Locate every blood parasite and identify its species.
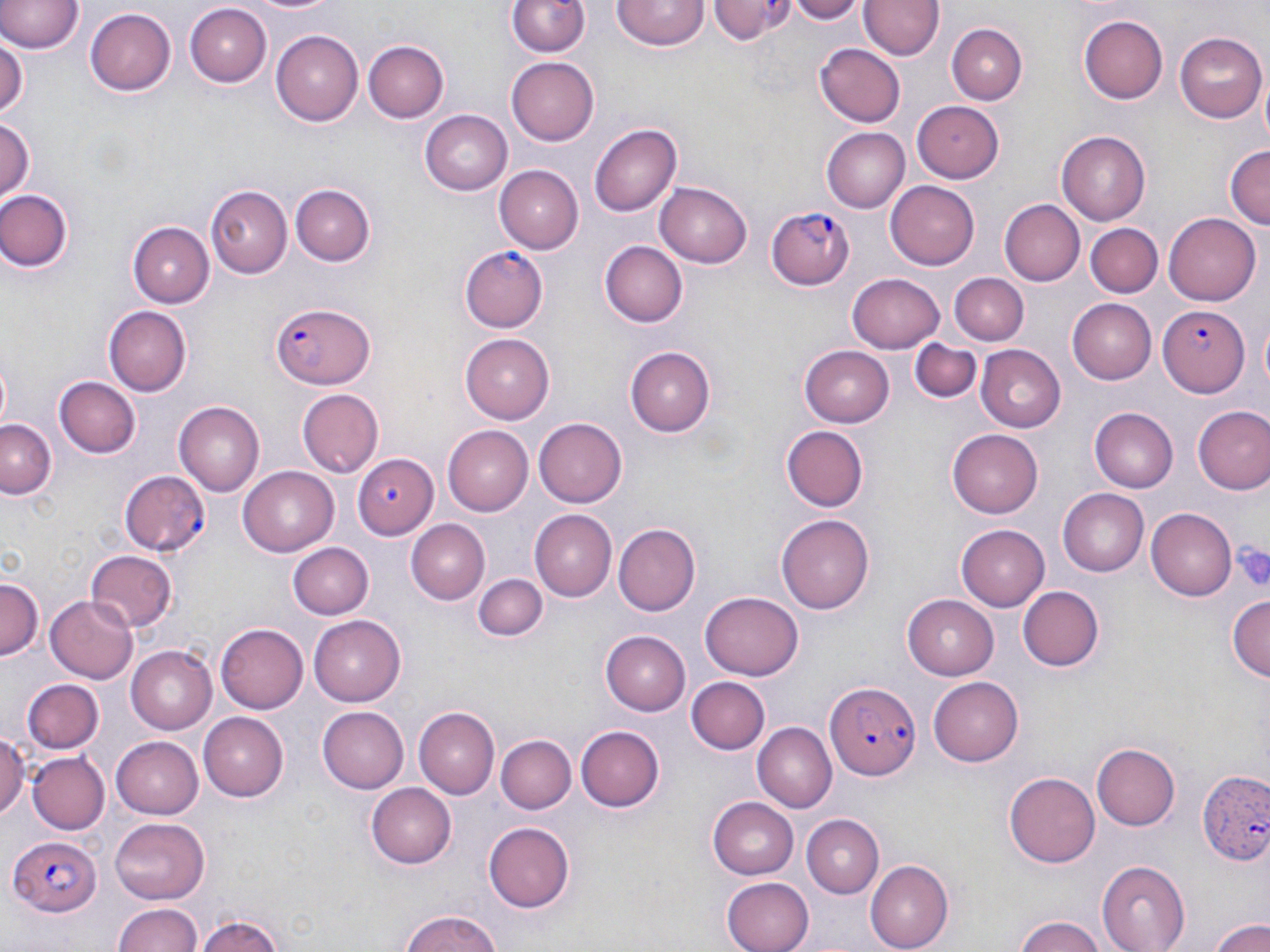

Approximate bounding boxes as (x1,y1)-(x2,y2) corner pairs in pixels.
Plasmodium falciparum-infected red blood cells: (767,205)-(857,290), (459,247)-(549,333), (271,299)-(378,390), (1158,304)-(1246,395), (351,453)-(439,539), (120,470)-(210,555), (827,683)-(921,779), (1199,771)-(1270,867), (11,834)-(104,918).
No Plasmodium ovale, Plasmodium malariae, Plasmodium vivax, Babesia divergens, or Trypanosoma brucei observed.

Summary:
  - Platelet locations: (1233,540)-(1270,591)
  - Uninfected red blood cell locations: (248,0)-(339,16), (507,0)-(591,57), (612,0)-(706,52), (708,0)-(797,44), (786,0)-(865,23), (0,1)-(82,55), (861,1)-(943,62), (186,3)-(271,85), (86,8)-(175,96), (1078,15)-(1168,103), (948,22)-(1029,103), (271,30)-(364,125), (1176,31)-(1266,121), (0,34)-(25,120), (362,40)-(447,123), (816,45)-(905,128), (507,59)-(599,145), (913,98)-(1003,182), (421,110)-(511,194), (0,116)-(37,203), (590,123)-(684,217), (820,126)-(909,212), (1057,131)-(1151,225), (1224,145)-(1270,232), (495,165)-(583,254), (654,181)-(753,268), (886,182)-(979,271), (291,184)-(374,266), (204,186)-(291,277), (0,188)-(74,273), (999,200)-(1084,286), (1164,212)-(1262,305), (128,221)-(213,307), (1085,224)-(1160,297), (598,240)-(686,327), (951,272)-(1028,343), (848,273)-(946,353), (1069,298)-(1160,384), (104,306)-(193,394), (459,333)-(552,422), (911,337)-(982,403), (801,345)-(895,427), (626,346)-(715,436), (976,346)-(1067,432), (0,355)-(12,432), (54,377)-(141,461), (296,389)-(384,479), (174,402)-(265,497), (1192,405)-(1270,492), (1091,409)-(1178,492), (534,417)-(627,507), (0,419)-(55,499), (781,425)-(868,513), (441,426)-(532,515), (948,430)-(1044,519), (240,467)-(338,555), (1057,488)-(1148,576), (1146,509)-(1236,599), (531,510)-(616,600), (778,513)-(878,612), (407,520)-(490,603), (613,522)-(701,613), (956,524)-(1050,611), (285,542)-(374,620), (85,550)-(177,632), (474,572)-(547,642), (0,573)-(44,657), (1017,585)-(1103,673), (700,592)-(804,680), (1226,593)-(1270,684), (45,594)-(137,684), (903,594)-(1001,679), (309,615)-(404,704), (217,622)-(308,713), (600,630)-(690,714), (126,645)-(216,734), (929,675)-(1023,766), (23,677)-(104,753), (687,677)-(769,755), (318,704)-(410,793), (414,706)-(497,800), (199,713)-(288,799), (755,721)-(838,811), (577,724)-(664,811), (0,728)-(25,820), (495,734)-(574,816), (113,736)-(203,817), (1091,741)-(1179,832), (27,751)-(109,834), (1005,772)-(1100,868), (363,783)-(457,867), (707,797)-(799,879), (110,815)-(211,902), (802,815)-(885,897), (485,823)-(576,910), (868,859)-(953,951), (1096,861)-(1190,951), (722,876)-(814,952), (114,902)-(204,952), (394,911)-(509,952), (197,913)-(287,952), (1013,914)-(1106,952), (1211,919)-(1270,952)
  - Slide-level diagnosis: Plasmodium falciparum
  - Magnification: 1000x
  - Stain: May-Grünwald-Giemsa
  - Modality: optical microscopy
  - Field of view: single
  - Image size: 1270×952 pixels
  - Preparation: thin blood smear